Report the malaria status of this cell.
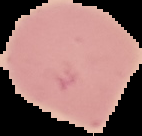

Uninfected.

From a thin blood smear. The area outside the segmented cell region is set to black. Image is 142×136 pixels.